Identify the blood parasite species.
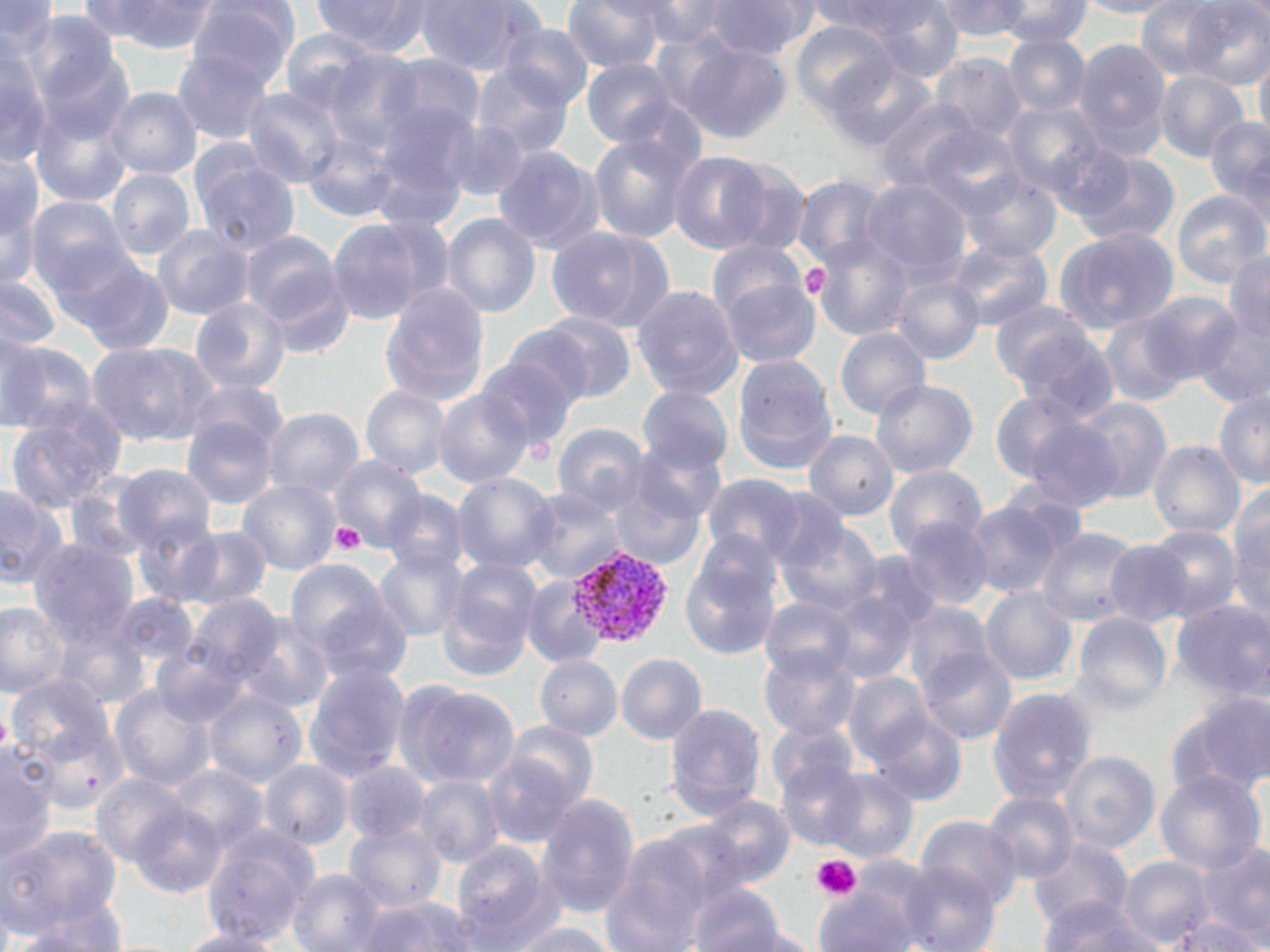
Plasmodium vivax.

image size = 1270×952 pixels
Plasmodium vivax-infected red blood cell locations = approximate bounding boxes as named x1/y1/x2/y2 corners in pixels: (x1=567, y1=543, x2=677, y2=650)
preparation = thin blood film
field of view = one of a larger specimen
stain = May-Grünwald-Giemsa
platelet locations = approximate bounding boxes as named x1/y1/x2/y2 corners in pixels: (x1=798, y1=264, x2=830, y2=299), (x1=331, y1=521, x2=364, y2=554), (x1=812, y1=854, x2=860, y2=900)
uninfected red blood cell locations = approximate bounding boxes as named x1/y1/x2/y2 corners in pixels: (x1=74, y1=0, x2=175, y2=43), (x1=187, y1=0, x2=302, y2=92), (x1=311, y1=0, x2=431, y2=54), (x1=414, y1=0, x2=540, y2=76), (x1=561, y1=0, x2=668, y2=73), (x1=626, y1=0, x2=731, y2=47), (x1=699, y1=0, x2=820, y2=60), (x1=807, y1=0, x2=935, y2=39), (x1=857, y1=0, x2=967, y2=82), (x1=931, y1=0, x2=1034, y2=41), (x1=1134, y1=0, x2=1227, y2=80), (x1=1181, y1=0, x2=1270, y2=89), (x1=0, y1=1, x2=59, y2=53), (x1=112, y1=1, x2=222, y2=54), (x1=996, y1=1, x2=1093, y2=47), (x1=1069, y1=1, x2=1183, y2=19), (x1=22, y1=9, x2=122, y2=102), (x1=789, y1=22, x2=898, y2=118), (x1=496, y1=24, x2=596, y2=109), (x1=278, y1=27, x2=386, y2=117), (x1=1003, y1=34, x2=1092, y2=117), (x1=1069, y1=35, x2=1174, y2=153), (x1=673, y1=38, x2=794, y2=146), (x1=0, y1=45, x2=52, y2=165), (x1=31, y1=48, x2=134, y2=146), (x1=174, y1=48, x2=272, y2=145), (x1=319, y1=50, x2=430, y2=150), (x1=930, y1=52, x2=1028, y2=143), (x1=377, y1=53, x2=486, y2=140), (x1=1253, y1=55, x2=1270, y2=148), (x1=259, y1=57, x2=397, y2=181), (x1=580, y1=57, x2=685, y2=149), (x1=821, y1=57, x2=940, y2=153), (x1=469, y1=63, x2=577, y2=159), (x1=1154, y1=70, x2=1249, y2=162), (x1=105, y1=87, x2=202, y2=179), (x1=240, y1=87, x2=347, y2=187), (x1=873, y1=97, x2=982, y2=193), (x1=367, y1=98, x2=479, y2=214), (x1=1002, y1=100, x2=1108, y2=197), (x1=31, y1=106, x2=132, y2=207), (x1=1203, y1=115, x2=1270, y2=215), (x1=440, y1=121, x2=532, y2=200), (x1=919, y1=124, x2=1025, y2=219), (x1=587, y1=130, x2=700, y2=244), (x1=300, y1=132, x2=400, y2=222), (x1=491, y1=144, x2=607, y2=254), (x1=1066, y1=147, x2=1181, y2=248), (x1=0, y1=148, x2=45, y2=242), (x1=190, y1=151, x2=301, y2=256), (x1=669, y1=151, x2=775, y2=253), (x1=106, y1=168, x2=196, y2=258), (x1=958, y1=170, x2=1061, y2=262), (x1=791, y1=176, x2=892, y2=269), (x1=861, y1=178, x2=973, y2=281), (x1=1, y1=183, x2=42, y2=292), (x1=1172, y1=190, x2=1270, y2=287), (x1=25, y1=196, x2=133, y2=293), (x1=440, y1=213, x2=542, y2=317), (x1=327, y1=217, x2=445, y2=324), (x1=545, y1=225, x2=674, y2=332), (x1=1054, y1=225, x2=1181, y2=334), (x1=152, y1=226, x2=254, y2=320), (x1=239, y1=230, x2=351, y2=344), (x1=809, y1=233, x2=916, y2=343), (x1=705, y1=238, x2=806, y2=322), (x1=945, y1=239, x2=1054, y2=332), (x1=1224, y1=250, x2=1270, y2=344), (x1=67, y1=254, x2=175, y2=355), (x1=888, y1=269, x2=985, y2=364), (x1=1, y1=276, x2=63, y2=352), (x1=718, y1=276, x2=820, y2=367), (x1=378, y1=282, x2=491, y2=406), (x1=631, y1=284, x2=745, y2=400), (x1=1135, y1=290, x2=1247, y2=386), (x1=191, y1=296, x2=292, y2=393), (x1=988, y1=299, x2=1097, y2=393), (x1=1097, y1=311, x2=1194, y2=408), (x1=1192, y1=311, x2=1270, y2=409), (x1=522, y1=312, x2=639, y2=405), (x1=1011, y1=324, x2=1120, y2=421), (x1=834, y1=327, x2=932, y2=419), (x1=0, y1=332, x2=46, y2=430), (x1=0, y1=338, x2=98, y2=437), (x1=87, y1=340, x2=215, y2=446), (x1=731, y1=354, x2=838, y2=474), (x1=473, y1=355, x2=578, y2=453), (x1=186, y1=378, x2=290, y2=456), (x1=871, y1=379, x2=978, y2=478), (x1=636, y1=385, x2=734, y2=473), (x1=361, y1=386, x2=453, y2=480), (x1=1213, y1=387, x2=1270, y2=489), (x1=432, y1=389, x2=535, y2=487), (x1=989, y1=390, x2=1093, y2=485), (x1=1068, y1=395, x2=1172, y2=504), (x1=260, y1=407, x2=365, y2=500), (x1=6, y1=411, x2=121, y2=511), (x1=181, y1=413, x2=279, y2=509), (x1=1020, y1=417, x2=1126, y2=509), (x1=551, y1=422, x2=650, y2=516), (x1=803, y1=429, x2=900, y2=520), (x1=624, y1=438, x2=727, y2=528), (x1=1147, y1=439, x2=1245, y2=537), (x1=326, y1=454, x2=428, y2=553), (x1=111, y1=463, x2=219, y2=555), (x1=883, y1=463, x2=988, y2=555), (x1=450, y1=472, x2=559, y2=573), (x1=701, y1=473, x2=808, y2=567), (x1=64, y1=474, x2=154, y2=561), (x1=607, y1=475, x2=707, y2=570), (x1=235, y1=480, x2=344, y2=576), (x1=1229, y1=482, x2=1270, y2=588), (x1=0, y1=483, x2=69, y2=588), (x1=379, y1=487, x2=471, y2=574), (x1=524, y1=487, x2=627, y2=582), (x1=760, y1=489, x2=854, y2=577), (x1=965, y1=496, x2=1082, y2=600), (x1=895, y1=516, x2=998, y2=609), (x1=134, y1=517, x2=225, y2=607), (x1=774, y1=517, x2=883, y2=616), (x1=1229, y1=522, x2=1270, y2=631), (x1=1144, y1=525, x2=1245, y2=621), (x1=169, y1=526, x2=274, y2=610), (x1=1036, y1=526, x2=1143, y2=625), (x1=28, y1=537, x2=140, y2=643), (x1=1103, y1=541, x2=1194, y2=626), (x1=373, y1=549, x2=469, y2=642), (x1=848, y1=549, x2=945, y2=634), (x1=678, y1=553, x2=781, y2=661), (x1=284, y1=559, x2=402, y2=662), (x1=438, y1=560, x2=541, y2=678), (x1=522, y1=578, x2=608, y2=668), (x1=978, y1=586, x2=1077, y2=685), (x1=822, y1=589, x2=918, y2=683), (x1=110, y1=592, x2=200, y2=670), (x1=179, y1=593, x2=289, y2=684), (x1=306, y1=593, x2=415, y2=686), (x1=760, y1=595, x2=858, y2=680), (x1=1171, y1=599, x2=1270, y2=702), (x1=0, y1=601, x2=69, y2=697), (x1=900, y1=602, x2=993, y2=690), (x1=230, y1=609, x2=337, y2=713), (x1=1071, y1=613, x2=1172, y2=711), (x1=52, y1=615, x2=152, y2=710), (x1=758, y1=644, x2=862, y2=740), (x1=915, y1=645, x2=1018, y2=746), (x1=153, y1=647, x2=247, y2=725), (x1=615, y1=653, x2=708, y2=745), (x1=533, y1=655, x2=623, y2=740), (x1=302, y1=662, x2=412, y2=781), (x1=841, y1=671, x2=935, y2=766), (x1=6, y1=673, x2=115, y2=767), (x1=396, y1=681, x2=519, y2=789), (x1=109, y1=683, x2=219, y2=791), (x1=987, y1=685, x2=1098, y2=803), (x1=202, y1=688, x2=309, y2=787), (x1=1172, y1=691, x2=1270, y2=796), (x1=663, y1=703, x2=767, y2=818), (x1=867, y1=711, x2=968, y2=805), (x1=764, y1=719, x2=859, y2=802), (x1=501, y1=722, x2=599, y2=811), (x1=30, y1=724, x2=124, y2=816), (x1=0, y1=743, x2=60, y2=859), (x1=1057, y1=750, x2=1161, y2=854), (x1=482, y1=751, x2=584, y2=847), (x1=258, y1=760, x2=353, y2=850), (x1=775, y1=760, x2=866, y2=851), (x1=341, y1=761, x2=433, y2=845), (x1=164, y1=766, x2=271, y2=854), (x1=817, y1=768, x2=920, y2=863), (x1=1155, y1=769, x2=1269, y2=874), (x1=92, y1=772, x2=192, y2=865), (x1=414, y1=775, x2=505, y2=868), (x1=981, y1=791, x2=1079, y2=883), (x1=535, y1=794, x2=641, y2=917), (x1=698, y1=795, x2=796, y2=887), (x1=128, y1=802, x2=229, y2=898), (x1=915, y1=814, x2=1022, y2=906), (x1=644, y1=819, x2=756, y2=907), (x1=343, y1=822, x2=446, y2=914), (x1=0, y1=824, x2=122, y2=935), (x1=200, y1=828, x2=319, y2=946), (x1=1028, y1=837, x2=1133, y2=931), (x1=449, y1=841, x2=560, y2=950), (x1=1199, y1=844, x2=1270, y2=944), (x1=602, y1=855, x2=710, y2=951), (x1=1117, y1=855, x2=1216, y2=948), (x1=895, y1=860, x2=1002, y2=952), (x1=287, y1=867, x2=386, y2=952), (x1=685, y1=882, x2=786, y2=952), (x1=812, y1=885, x2=920, y2=952), (x1=356, y1=896, x2=480, y2=951), (x1=1037, y1=897, x2=1158, y2=952), (x1=16, y1=903, x2=126, y2=952), (x1=1166, y1=917, x2=1268, y2=952), (x1=512, y1=922, x2=619, y2=952), (x1=710, y1=925, x2=828, y2=952), (x1=175, y1=929, x2=288, y2=952)
magnification = 1000x
modality = optical microscopy